Name the parasite shown.
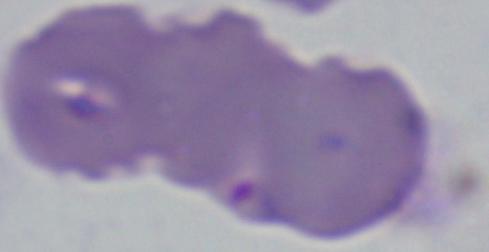

Babesia.

Micrograph. Captured at 1000x magnification.